Point out each Plasmodium parasite.
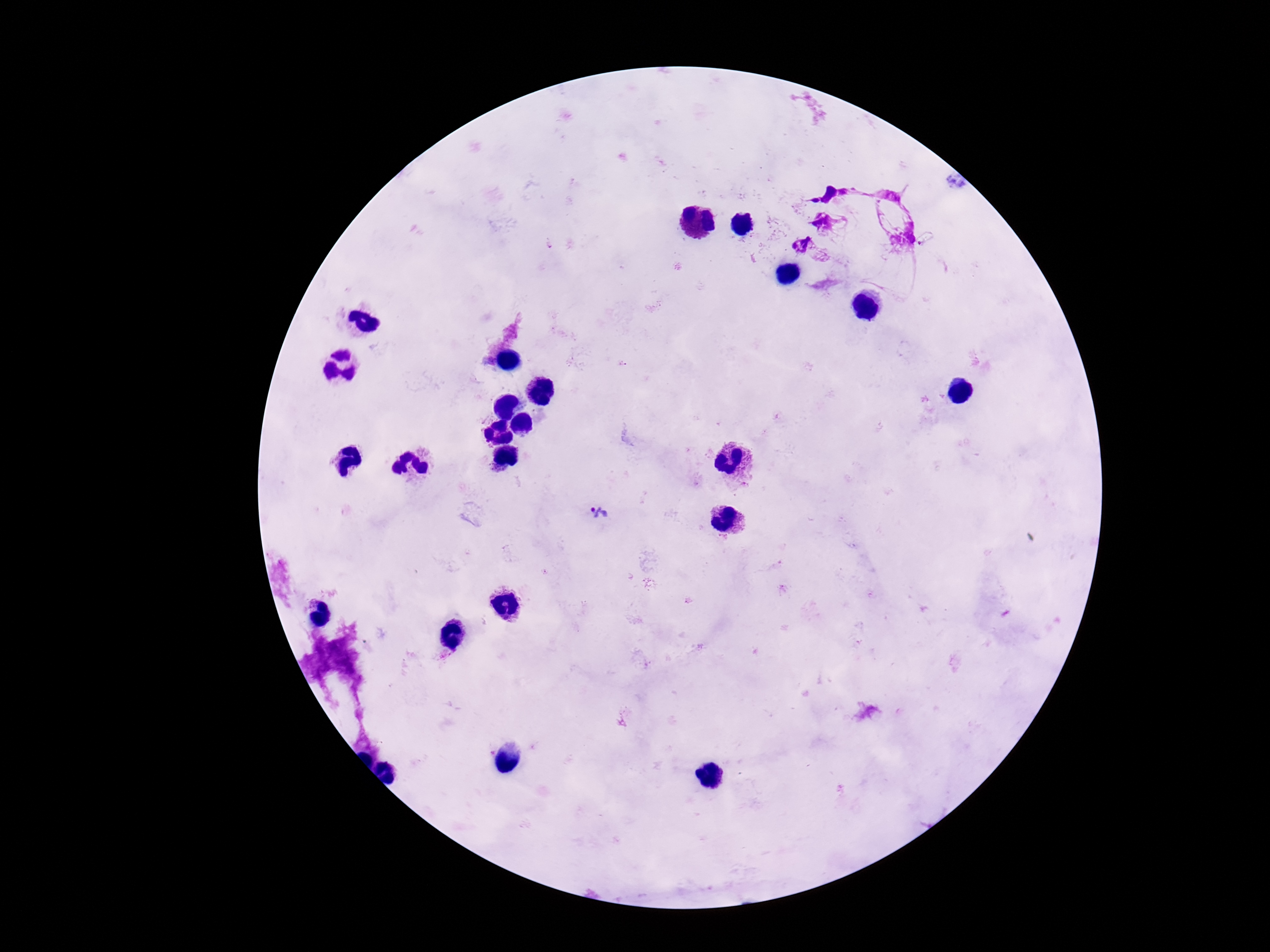

Approximate centers as [x, y] in pixels.
Plasmodium parasites: [929, 241], [598, 514].

preparation: thick peripheral-blood smear
capture: smartphone camera through the microscope eyepiece
field_of_view: one from this slide
stain: Giemsa
image_size: 1270×952 pixels
patient_malaria_status: positive
magnification: 100x